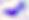

identification = Toxoplasma gondii
magnification = 400x
modality = photomicrograph